Classify this cell by malaria status.
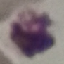

It is uninfected.

Automatically extracted cell patch, resized to 64 × 64 pixels. Giemsa-stained preparation. Acquired by smartphone through the microscope eyepiece. Thin blood film.